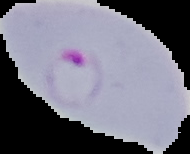
Image is 190×154 pixels. The area outside the segmented cell region is set to black. Malaria status: parasitized. From a thin blood smear.